Evaluate for malaria.
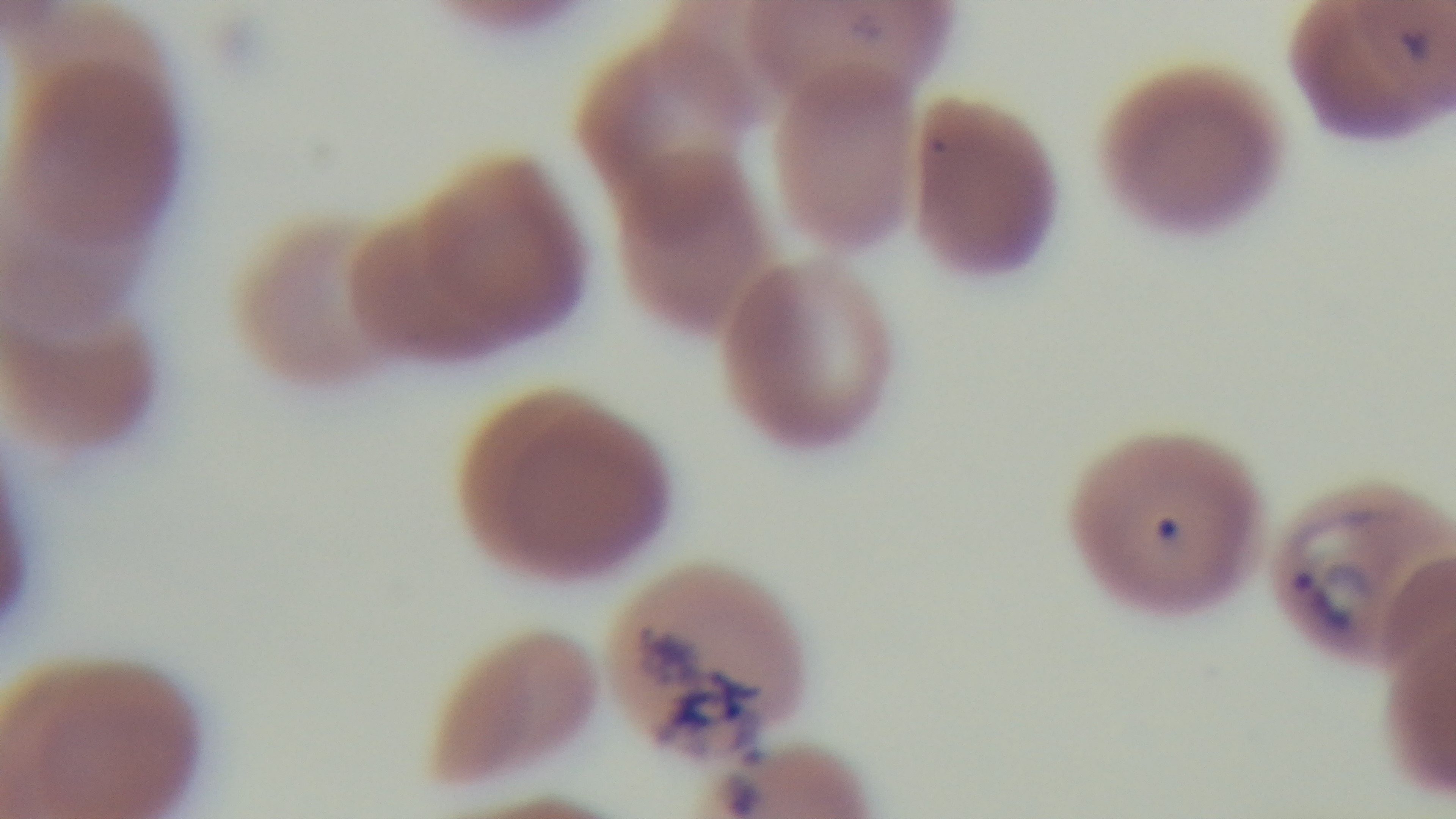
Infected.

Summary:
  - Field of view: single
  - Objective: 100x oil immersion
  - Preparation: thin blood film
  - Capture: mounted 4K digital camera
  - Modality: light microscopy
  - Stain: Giemsa